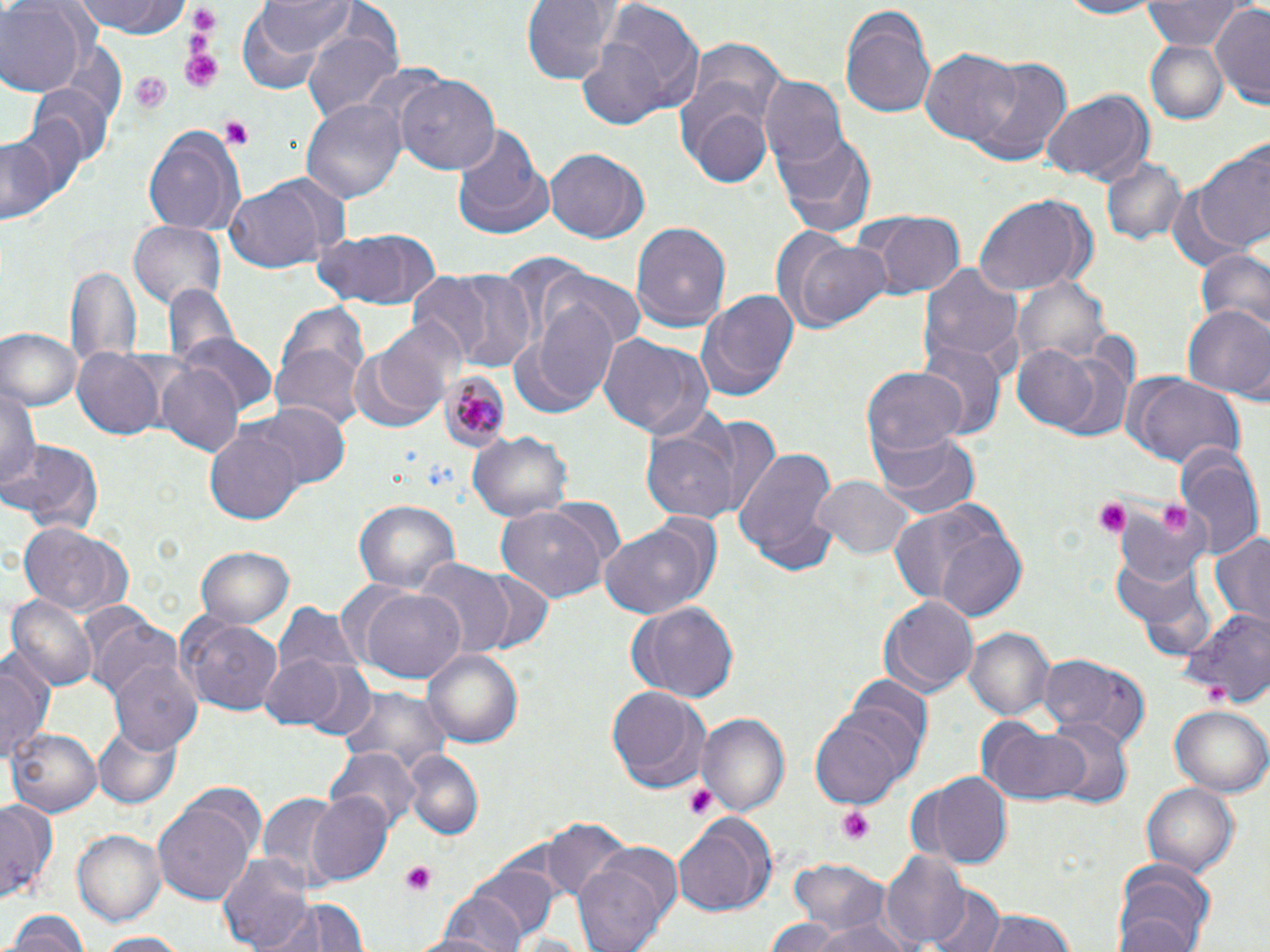
Summary:
  - Coordinate format: approximate bounding boxes as [x1, y1, x2, y2] in pixels
  - Uninfected red blood cell locations: [74, 0, 193, 41], [522, 0, 617, 86], [1044, 0, 1168, 18], [1145, 0, 1242, 50], [257, 1, 358, 57], [837, 2, 939, 119], [0, 4, 83, 97], [1210, 5, 1270, 107], [582, 6, 706, 125], [301, 27, 403, 122], [687, 38, 789, 135], [1147, 41, 1226, 121], [921, 49, 1020, 149], [964, 56, 1072, 166], [357, 65, 446, 148], [397, 75, 501, 177], [758, 77, 848, 170], [28, 86, 110, 174], [678, 88, 775, 189], [1043, 93, 1151, 184], [302, 100, 405, 204], [13, 112, 91, 216], [450, 121, 551, 236], [141, 124, 245, 235], [773, 129, 877, 238], [0, 135, 59, 224], [1194, 147, 1270, 256], [545, 149, 648, 243], [1101, 158, 1190, 248], [221, 180, 337, 273], [1165, 186, 1254, 273], [972, 194, 1096, 298], [854, 211, 965, 298], [130, 221, 226, 308], [631, 221, 733, 332], [311, 228, 441, 311], [776, 232, 895, 335], [1192, 244, 1269, 335], [65, 261, 141, 380], [920, 263, 1024, 372], [438, 268, 536, 370], [545, 269, 645, 353], [406, 270, 499, 361], [1013, 275, 1110, 370], [163, 284, 238, 374], [695, 285, 800, 403], [273, 301, 369, 423], [525, 303, 621, 406], [1181, 304, 1270, 402], [376, 316, 468, 411], [1, 328, 80, 411], [179, 332, 275, 417], [596, 334, 712, 438], [346, 338, 446, 434], [1008, 342, 1107, 435], [919, 344, 1005, 442], [71, 347, 166, 441], [153, 361, 246, 458], [862, 362, 967, 463], [1120, 371, 1246, 471], [1, 379, 42, 502], [252, 403, 349, 489], [692, 415, 781, 516], [641, 424, 743, 525], [204, 426, 302, 525], [871, 430, 982, 521], [469, 431, 573, 521], [3, 438, 104, 535], [735, 446, 838, 574], [1174, 449, 1263, 561], [813, 476, 913, 562], [354, 500, 461, 599], [896, 500, 1027, 616], [1114, 500, 1212, 589], [497, 507, 605, 602], [598, 518, 718, 620], [18, 520, 133, 618], [1211, 531, 1270, 629], [195, 543, 294, 628], [1115, 559, 1219, 663], [411, 561, 517, 660], [354, 583, 467, 684], [9, 595, 98, 692], [878, 595, 978, 698], [625, 600, 740, 700], [1179, 611, 1270, 705], [177, 614, 283, 715], [87, 617, 184, 706], [965, 628, 1055, 722], [420, 646, 524, 749], [0, 650, 54, 768], [257, 652, 352, 730], [1037, 652, 1150, 750], [110, 660, 204, 754], [296, 661, 379, 745], [605, 685, 711, 793], [337, 688, 454, 770], [1171, 704, 1270, 796], [807, 710, 914, 806], [696, 712, 790, 815], [1045, 719, 1132, 808], [975, 720, 1094, 806], [94, 724, 183, 809], [8, 727, 102, 819], [326, 749, 422, 832], [404, 751, 482, 840], [923, 773, 1010, 867], [1142, 781, 1239, 880], [255, 792, 342, 889], [308, 792, 391, 882], [153, 796, 257, 907], [0, 799, 58, 904], [673, 816, 779, 916], [544, 822, 633, 907], [74, 830, 165, 924], [572, 847, 683, 951], [883, 852, 971, 950], [218, 853, 315, 952], [787, 861, 896, 939], [469, 863, 561, 942], [1114, 868, 1217, 952], [930, 886, 1005, 952], [423, 897, 525, 951], [255, 899, 370, 952], [6, 909, 88, 952], [976, 909, 1080, 952], [761, 915, 846, 952], [810, 915, 917, 952], [508, 931, 593, 952], [93, 932, 188, 951]
  - Plasmodium malariae-infected red blood cell locations: [441, 370, 512, 452]
  - Platelet locations: [187, 8, 222, 42], [179, 48, 224, 95], [127, 71, 172, 112], [219, 117, 253, 147], [1093, 498, 1131, 538], [1205, 680, 1236, 708], [686, 784, 721, 821], [835, 806, 878, 842], [401, 861, 438, 898]
  - Slide-level diagnosis: Plasmodium malariae
  - Field of view: single
  - Stain: May-Grünwald-Giemsa
  - Preparation: thin blood film
  - Magnification: 1000x
  - Image size: 1270×952 pixels
  - Modality: optical microscopy